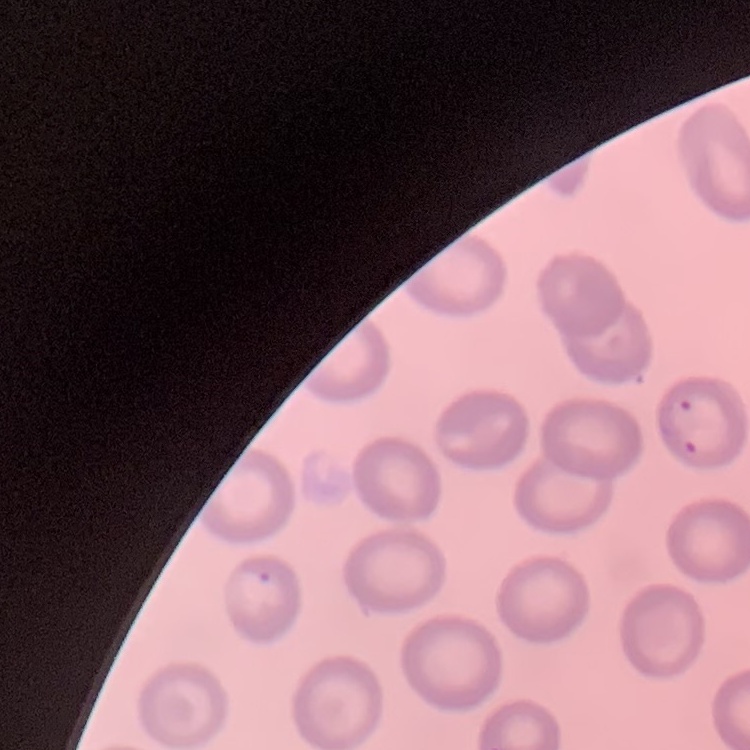

The red blood cells show no rouleaux formation. Square crop of a larger photomicrograph. Stained with either Field's or Giemsa. Thin peripheral smear.